Assess this cell for malaria.
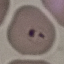
Parasitized.

Giemsa stain. Thin smear of blood. Automatically extracted cell patch, resized to 64 × 64 pixels. Photographed with a smartphone camera at the microscope eyepiece.